State which parasite is depicted.
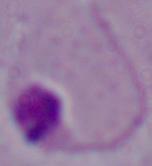

Leishmania.

Summary:
  - Magnification: 1000x
  - Modality: micrograph